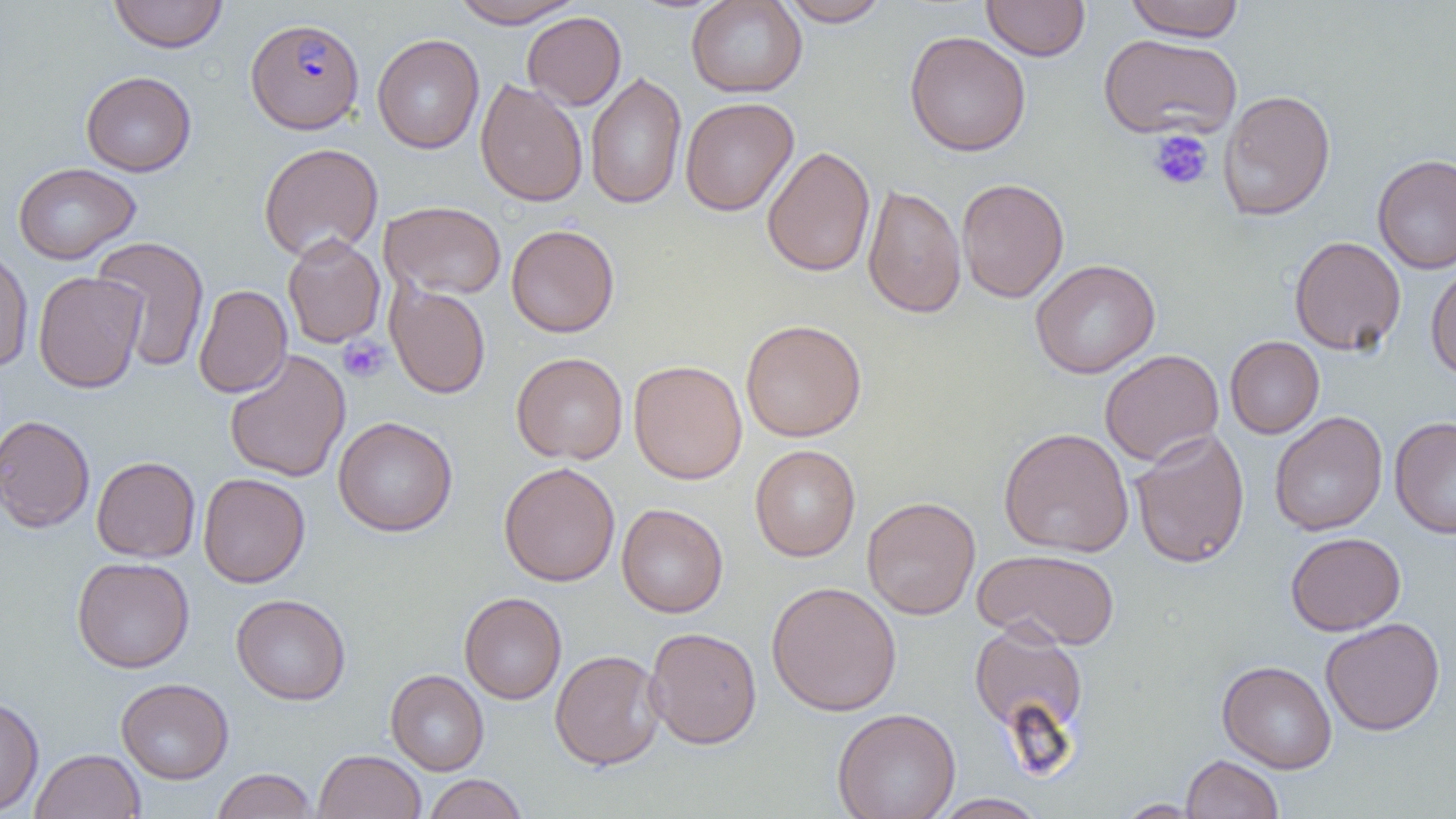

Summary:
  - Coordinate format: approximate bounding boxes as [x1, y1, x2, y2] in pixels
  - Plasmodium falciparum-infected red blood cell locations: [246, 17, 364, 134]
  - Uninfected red blood cell locations: [108, 0, 228, 53], [449, 0, 583, 28], [686, 0, 807, 98], [779, 0, 890, 27], [981, 0, 1090, 61], [1125, 0, 1245, 42], [522, 11, 626, 110], [904, 30, 1031, 157], [1098, 33, 1242, 140], [372, 34, 484, 153], [80, 71, 197, 176], [585, 72, 687, 210], [475, 79, 588, 208], [1219, 89, 1335, 221], [680, 97, 798, 216], [258, 142, 384, 261], [761, 145, 876, 277], [1372, 154, 1456, 275], [12, 162, 140, 264], [956, 177, 1069, 303], [862, 184, 966, 319], [379, 200, 507, 299], [506, 224, 619, 337], [282, 233, 385, 349], [92, 235, 210, 372], [1289, 235, 1406, 355], [0, 246, 34, 373], [1030, 259, 1160, 379], [1426, 263, 1456, 380], [32, 271, 146, 393], [385, 282, 491, 400], [193, 284, 292, 398], [741, 319, 867, 442], [1225, 336, 1325, 438], [1099, 349, 1224, 466], [224, 350, 351, 483], [511, 352, 628, 464], [628, 360, 748, 484], [1269, 411, 1388, 536], [0, 415, 95, 533], [332, 416, 458, 537], [1390, 416, 1456, 538], [998, 427, 1134, 557], [1130, 428, 1250, 569], [750, 444, 860, 561], [91, 456, 200, 562], [498, 461, 620, 586], [198, 472, 310, 588], [862, 496, 981, 620], [616, 503, 728, 618], [1285, 532, 1406, 636], [973, 548, 1120, 651], [72, 556, 194, 673], [766, 581, 902, 716], [459, 592, 567, 704], [231, 593, 350, 705], [1320, 618, 1445, 736], [968, 622, 1089, 739], [644, 626, 762, 749], [550, 649, 666, 770], [1217, 660, 1337, 773], [385, 669, 489, 775], [116, 677, 234, 784], [0, 696, 44, 815], [832, 708, 961, 819], [31, 749, 145, 819], [313, 749, 427, 819], [1181, 754, 1283, 818], [211, 768, 317, 819], [423, 774, 528, 818], [929, 793, 1049, 818], [1115, 799, 1205, 818]
  - Platelet locations: [1148, 129, 1214, 191], [337, 337, 389, 383]
  - Slide-level diagnosis: Plasmodium falciparum
  - Field of view: one of a larger specimen
  - Magnification: 1000x
  - Image size: 1456×819 pixels
  - Preparation: thin blood smear
  - Modality: optical microscopy